Locate every Babesia divergens-infected red blood cell.
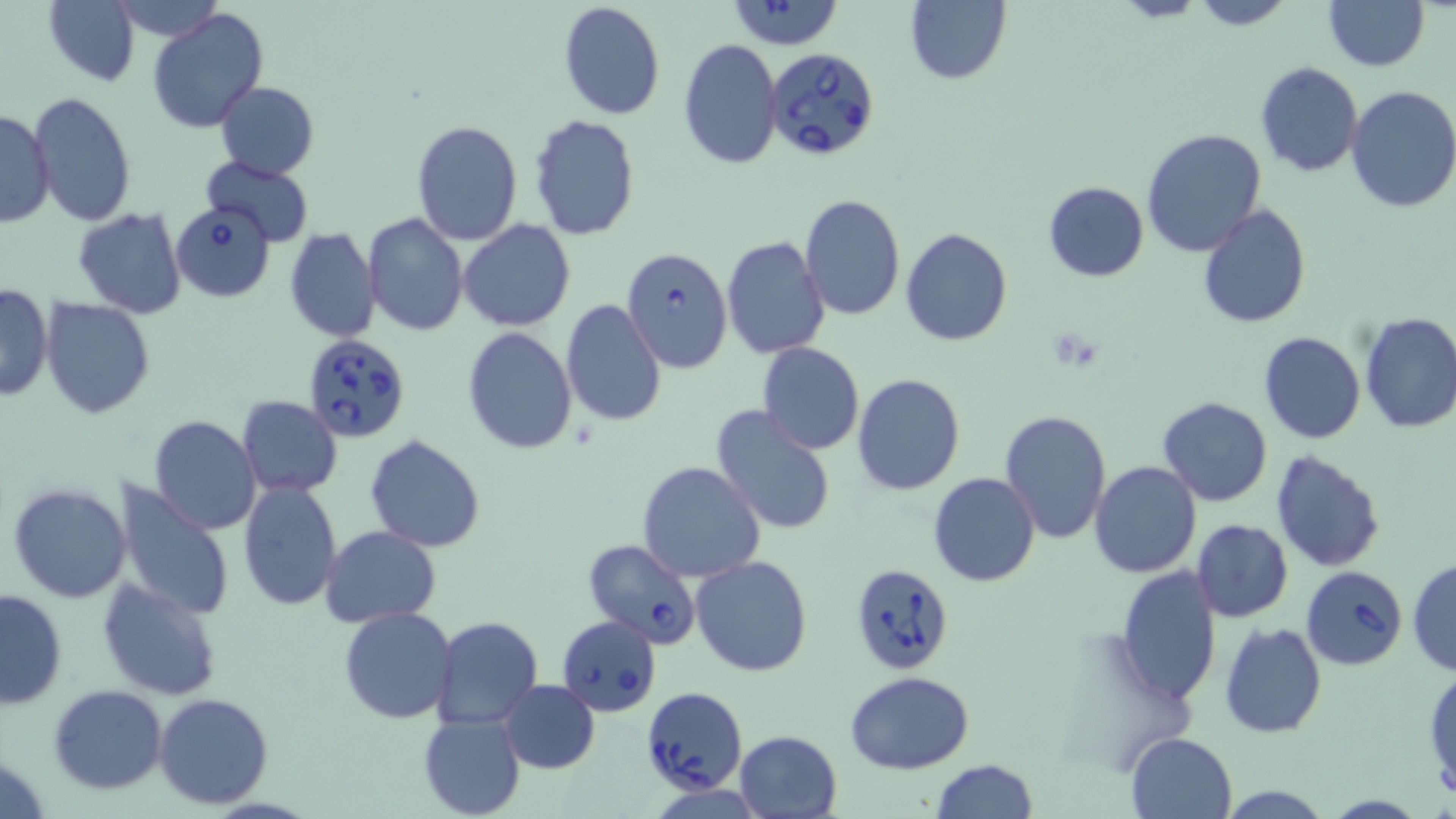
Approximate bounding boxes as (x1,y1)-(x2,y2) corner pairs in pixels.
Babesia divergens-infected red blood cells: (724,1)-(846,49), (765,50)-(881,162), (170,202)-(276,301), (622,247)-(735,374), (301,333)-(411,442), (583,539)-(703,648), (850,564)-(955,674), (1301,566)-(1407,670), (556,616)-(661,715), (642,687)-(747,794).

Summary:
  - Uninfected red blood cell locations: (1188,0)-(1296,29), (43,1)-(140,86), (558,1)-(665,119), (904,1)-(1011,85), (1323,2)-(1430,72), (146,7)-(269,133), (679,37)-(783,171), (1254,63)-(1365,177), (215,81)-(320,179), (1344,86)-(1456,213), (27,92)-(137,228), (0,108)-(55,229), (530,114)-(641,242), (410,121)-(522,245), (1141,128)-(1267,257), (201,156)-(315,247), (1043,181)-(1148,282), (799,194)-(905,321), (1197,204)-(1311,328), (72,208)-(187,319), (361,213)-(468,336), (459,219)-(575,331), (284,228)-(379,343), (900,229)-(1013,346), (721,236)-(830,357), (0,284)-(53,403), (41,299)-(155,420), (559,300)-(667,427), (1358,311)-(1456,434), (463,327)-(577,453), (1259,331)-(1366,444), (758,342)-(865,454), (852,373)-(964,495), (1156,396)-(1273,507), (238,397)-(342,497), (710,404)-(838,538), (1000,408)-(1112,545), (148,415)-(262,536), (364,434)-(485,552), (1270,448)-(1389,572), (637,461)-(767,584), (1088,461)-(1203,578), (928,473)-(1039,587), (238,479)-(343,612), (111,480)-(235,621), (7,483)-(130,604), (1191,518)-(1293,621), (319,526)-(441,629), (690,556)-(814,675), (1408,559)-(1456,675), (1114,566)-(1223,706), (97,578)-(221,701), (0,589)-(68,709), (338,605)-(459,725), (430,616)-(542,730), (1219,621)-(1327,739), (1424,667)-(1455,802), (845,671)-(975,774), (499,679)-(600,774), (47,685)-(168,795), (154,693)-(273,810), (418,712)-(525,819), (735,730)-(841,817), (1126,731)-(1236,817), (930,760)-(1038,818)
  - Slide-level diagnosis: Babesia divergens
  - Field of view: single
  - Magnification: 1000x
  - Image size: 1456×819 pixels
  - Stain: May-Grünwald-Giemsa
  - Preparation: thin blood smear
  - Modality: optical microscopy